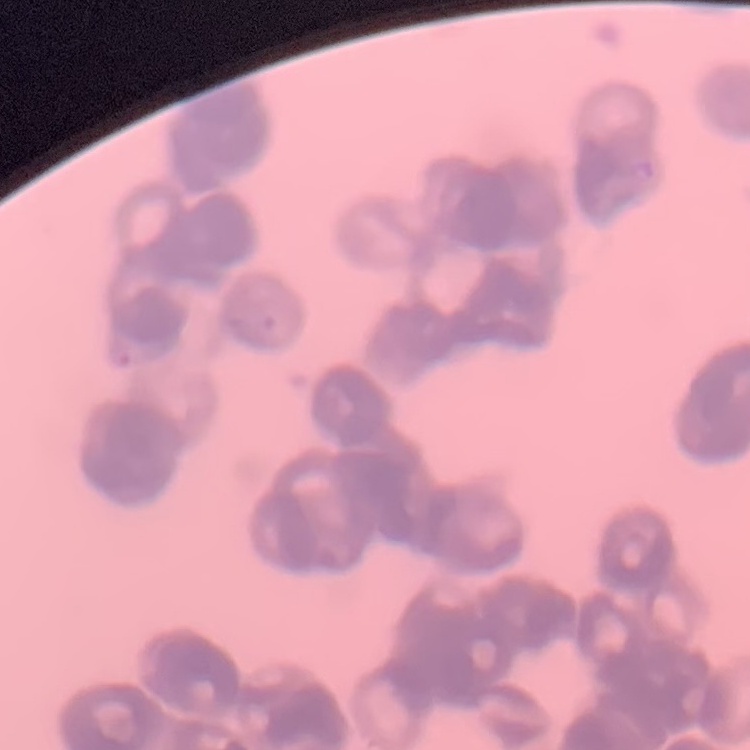

Summary:
  - Red blood cell morphology: rouleaux formation
  - Image type: one tile cut from a larger photomicrograph
  - Stain: Field's or Giemsa
  - Preparation: thin blood smear